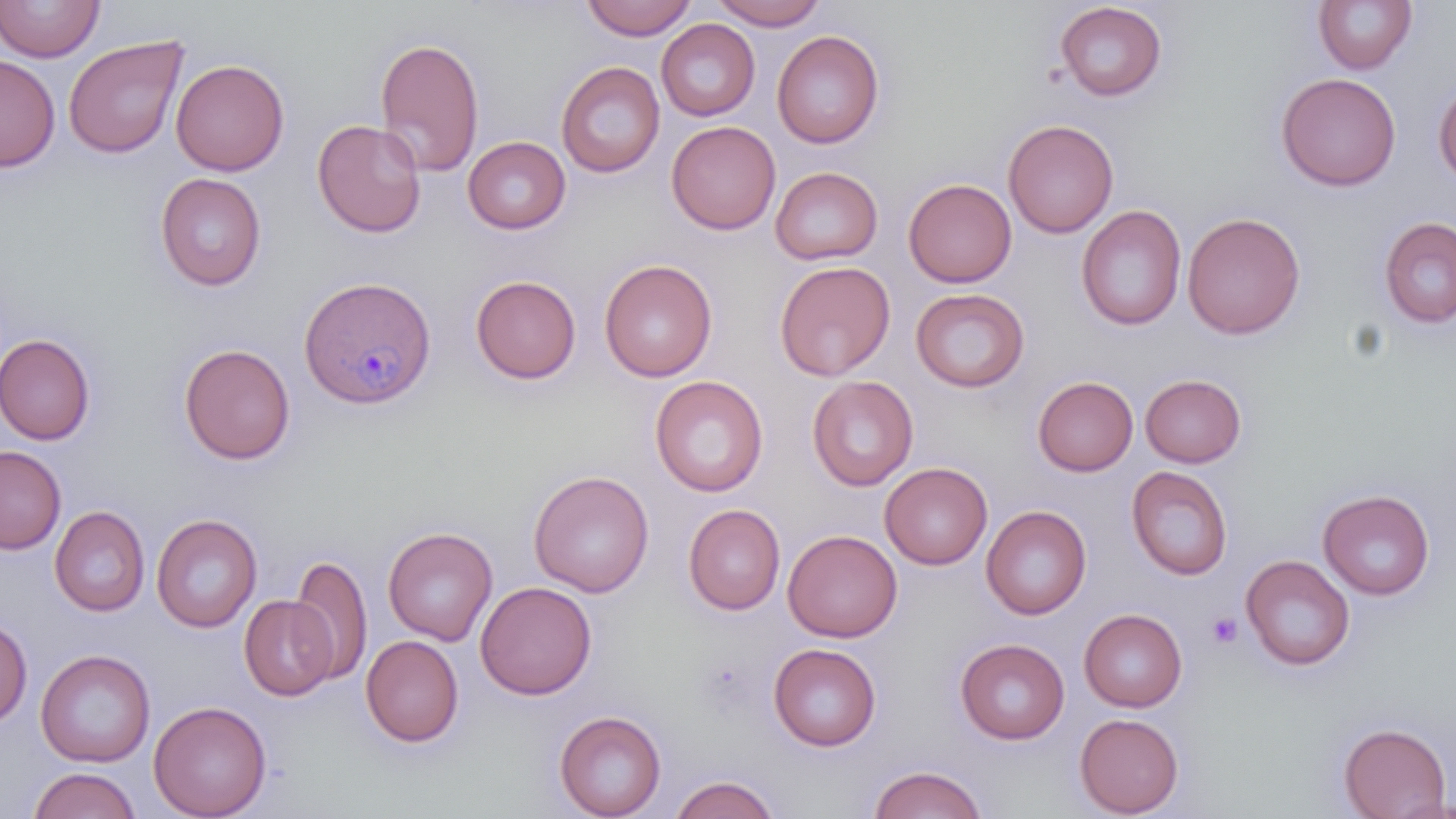

{
  "slide_level_diagnosis": "Plasmodium malariae",
  "uninfected_red_blood_cell_locations": "approximate bounding boxes as (x1, y1, x2, y2) in pixels: (0, 0, 104, 62), (579, 0, 698, 40), (710, 0, 827, 29), (1054, 1, 1168, 102), (1313, 1, 1417, 75), (656, 19, 760, 121), (772, 30, 885, 149), (63, 34, 189, 159), (375, 36, 485, 176), (0, 53, 60, 172), (171, 59, 289, 176), (556, 61, 665, 178), (1276, 72, 1401, 191), (1433, 79, 1456, 187), (312, 118, 427, 237), (1003, 119, 1118, 238), (666, 120, 781, 235), (462, 136, 571, 235), (770, 166, 883, 265), (155, 172, 267, 290), (903, 178, 1017, 287), (1076, 204, 1187, 331), (1182, 212, 1305, 339), (1378, 216, 1456, 328), (599, 258, 717, 382), (774, 261, 895, 381), (470, 275, 581, 384), (910, 288, 1030, 392), (0, 333, 96, 445), (179, 342, 296, 465), (1140, 373, 1247, 467), (649, 375, 768, 497), (806, 375, 918, 491), (1032, 375, 1138, 476), (0, 445, 66, 554), (879, 462, 992, 569), (1126, 465, 1233, 580), (528, 470, 654, 597), (1317, 488, 1436, 599), (682, 503, 786, 615), (49, 505, 150, 616), (980, 505, 1091, 620), (151, 513, 262, 632), (382, 526, 498, 645), (783, 529, 902, 642), (290, 555, 373, 685), (1240, 555, 1355, 671), (475, 581, 597, 700), (239, 596, 338, 700), (1078, 608, 1188, 712), (0, 618, 32, 726), (361, 635, 464, 747), (955, 638, 1070, 744), (768, 643, 881, 751), (35, 649, 156, 767), (149, 700, 272, 819), (554, 710, 667, 819), (1074, 713, 1184, 817), (1337, 722, 1451, 819), (868, 765, 987, 818), (28, 767, 141, 819), (669, 774, 780, 819), (1383, 793, 1456, 818)",
  "stain": "May-Grünwald-Giemsa",
  "preparation": "thin blood smear",
  "plasmodium_malariae_infected_red_blood_cell_locations": "approximate bounding boxes as (x1, y1, x2, y2) in pixels: (300, 276, 437, 410)",
  "field_of_view": "one of a larger specimen",
  "modality": "light microscopy",
  "platelet_locations": "approximate bounding boxes as (x1, y1, x2, y2) in pixels: (1206, 612, 1243, 650)",
  "image_size": "1456×819 pixels",
  "magnification": "1000x"
}